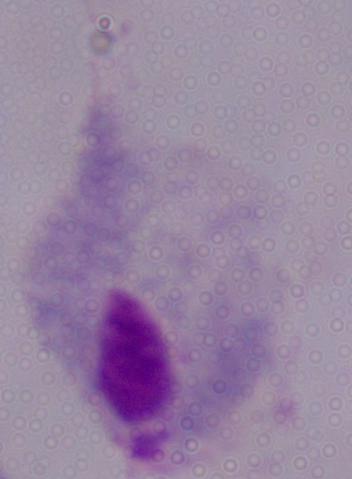
Summary:
  - Modality: photomicrograph
  - Magnification: 1000x
  - Identification: trichomonad